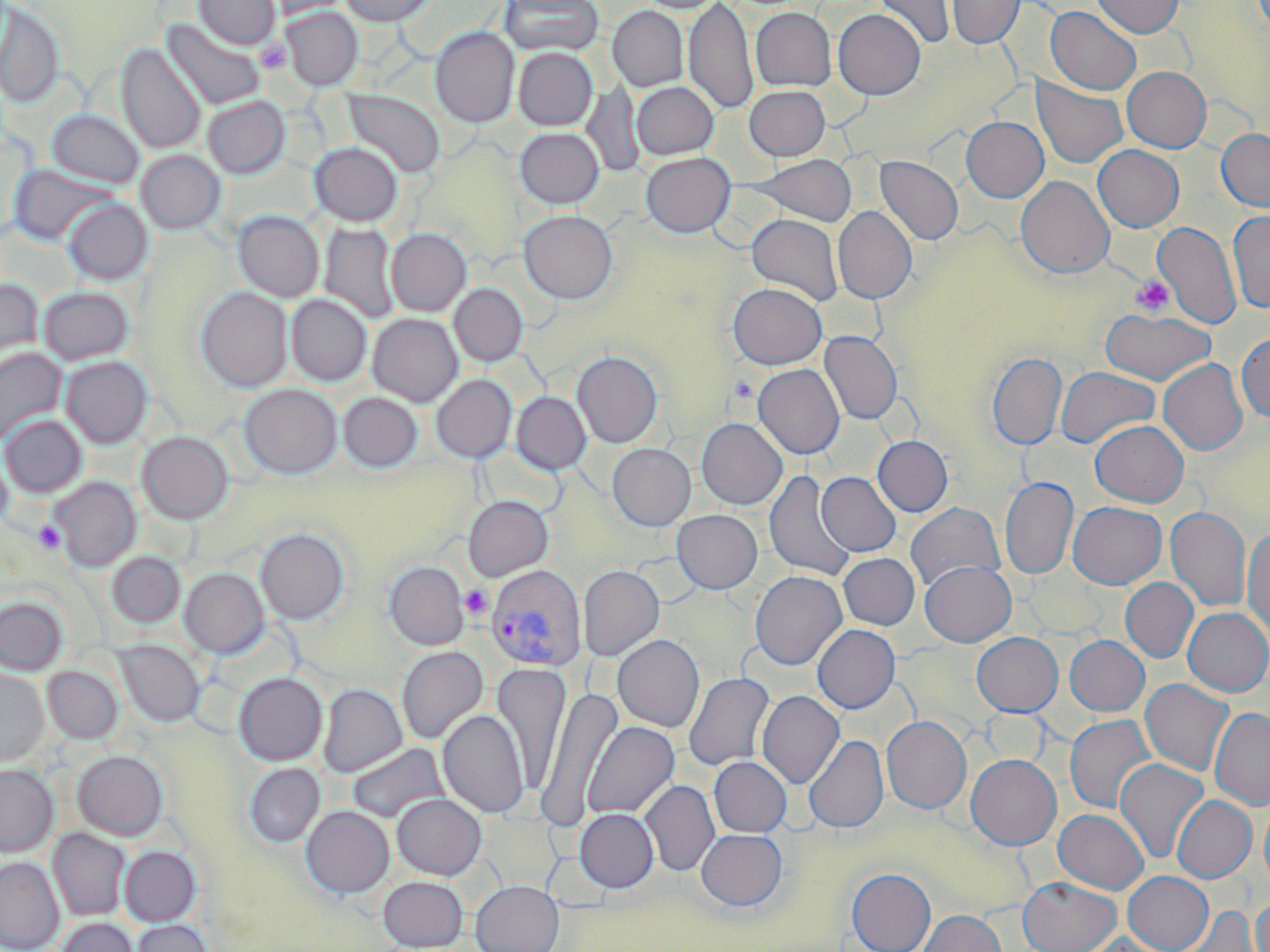

Approximate bounding boxes as (x1,y1)-(x2,y2) corner pairs in pixels. Platelet locations: (255,40)-(292,75), (1130,275)-(1174,316), (728,375)-(758,403), (34,521)-(63,554), (460,584)-(492,619). Plasmodium vivax-infected red blood cell locations: (486,564)-(586,670). Uninfected red blood cell locations: (194,0)-(280,50), (263,0)-(353,19), (339,0)-(436,26), (500,0)-(604,57), (637,0)-(725,13), (684,0)-(757,116), (874,0)-(955,50), (947,0)-(1024,49), (1091,0)-(1184,38), (0,2)-(65,108), (608,6)-(688,91), (1045,6)-(1141,95), (281,8)-(363,90), (751,8)-(836,91), (833,9)-(926,99), (162,18)-(265,110), (430,27)-(520,128), (116,43)-(206,154), (513,48)-(597,130), (1122,67)-(1211,152), (1032,79)-(1128,168), (582,81)-(645,178), (632,82)-(719,159), (745,85)-(831,160), (343,90)-(445,178), (203,96)-(290,179), (46,109)-(144,190), (961,116)-(1048,202), (514,127)-(604,208), (1217,129)-(1270,212), (309,142)-(402,225), (1093,145)-(1184,232), (136,150)-(226,235), (641,152)-(735,238), (747,154)-(858,226), (875,156)-(963,245), (8,164)-(116,247), (1015,175)-(1114,279), (63,199)-(152,285), (833,206)-(917,304), (519,210)-(618,304), (233,211)-(324,302), (1228,211)-(1270,313), (746,213)-(844,305), (1154,221)-(1240,330), (319,223)-(400,324), (386,228)-(471,316), (0,279)-(44,373), (449,283)-(527,366), (727,283)-(827,369), (39,286)-(134,365), (196,288)-(292,392), (286,295)-(371,386), (1101,308)-(1215,386), (368,313)-(463,406), (819,331)-(902,425), (1236,333)-(1270,421), (0,348)-(67,445), (572,351)-(663,448), (987,352)-(1067,450), (61,356)-(152,449), (1158,359)-(1247,456), (753,363)-(845,459), (1056,366)-(1160,448), (431,375)-(516,463), (239,384)-(342,479), (338,392)-(422,472), (511,392)-(591,475), (1,415)-(87,497), (697,418)-(787,510), (1090,420)-(1188,507), (137,432)-(233,524), (872,435)-(953,516), (607,443)-(696,531), (0,445)-(13,534), (764,470)-(856,581), (817,472)-(901,557), (1000,476)-(1078,580), (50,477)-(141,572), (464,496)-(553,581), (1068,501)-(1166,589), (905,502)-(1004,592), (1165,506)-(1251,611), (671,510)-(763,594), (1243,527)-(1270,639), (255,528)-(349,625), (107,551)-(185,629), (838,552)-(919,630), (384,561)-(469,649), (920,561)-(1016,647), (578,565)-(665,660), (180,567)-(269,658), (750,570)-(847,670), (1120,578)-(1198,662), (0,596)-(67,675), (1183,608)-(1270,696), (812,624)-(900,713), (971,632)-(1062,716), (612,634)-(705,732), (1064,635)-(1149,715), (116,641)-(205,728), (397,646)-(488,744), (491,663)-(572,796), (43,665)-(122,745), (0,666)-(48,767), (683,672)-(775,772), (234,673)-(327,765), (1140,679)-(1234,776), (318,684)-(407,777), (538,687)-(622,827), (757,690)-(844,788), (1210,707)-(1270,810), (438,709)-(529,818), (1065,714)-(1157,814), (882,716)-(971,813), (583,721)-(679,819), (804,734)-(888,833), (347,743)-(449,824), (73,751)-(168,840), (966,754)-(1061,850), (709,756)-(792,837), (1114,759)-(1208,863), (243,763)-(325,847), (0,764)-(58,857), (640,779)-(720,877), (391,793)-(486,880), (1172,796)-(1256,882), (1259,798)-(1270,894), (301,806)-(394,898), (574,808)-(659,892), (1053,809)-(1149,893), (482,814)-(558,890), (48,828)-(130,921), (696,829)-(787,911), (120,846)-(201,925), (0,858)-(64,951), (847,868)-(936,952), (1123,872)-(1213,951), (379,876)-(467,951), (1018,877)-(1120,952), (471,880)-(564,952), (1251,895)-(1270,952), (1178,905)-(1262,952), (917,910)-(1006,952), (57,917)-(138,952), (130,919)-(213,952), (1077,931)-(1172,952). Slide-level diagnosis: Plasmodium vivax. Image is 1270×952 pixels. May-Grünwald-Giemsa stain. Thin blood smear. Captured at 1000x magnification. Optical microscopy. Single field of view.